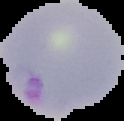

Summary:
  - Image size: 124×121 pixels
  - Malaria status: parasitized
  - Image type: segmented cell region with the area outside set to black
  - Preparation: thin blood smear